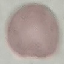

result: negative for malaria parasites
capture: smartphone through the microscope eyepiece
preparation: thin smear
stain: Giemsa
image_type: automatically extracted cell patch, resized to 64 × 64 pixels